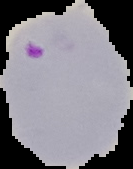 From a thin blood film. Result: Plasmodium parasites detected. Segmented cell region on a black background. Image is 133×169 pixels.